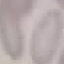
result = no malaria parasites detected
image type = cell patch, automatically extracted from a larger field of view and resized to 64 × 64 pixels
preparation = thin blood film
capture = smartphone through the microscope eyepiece
stain = Giemsa